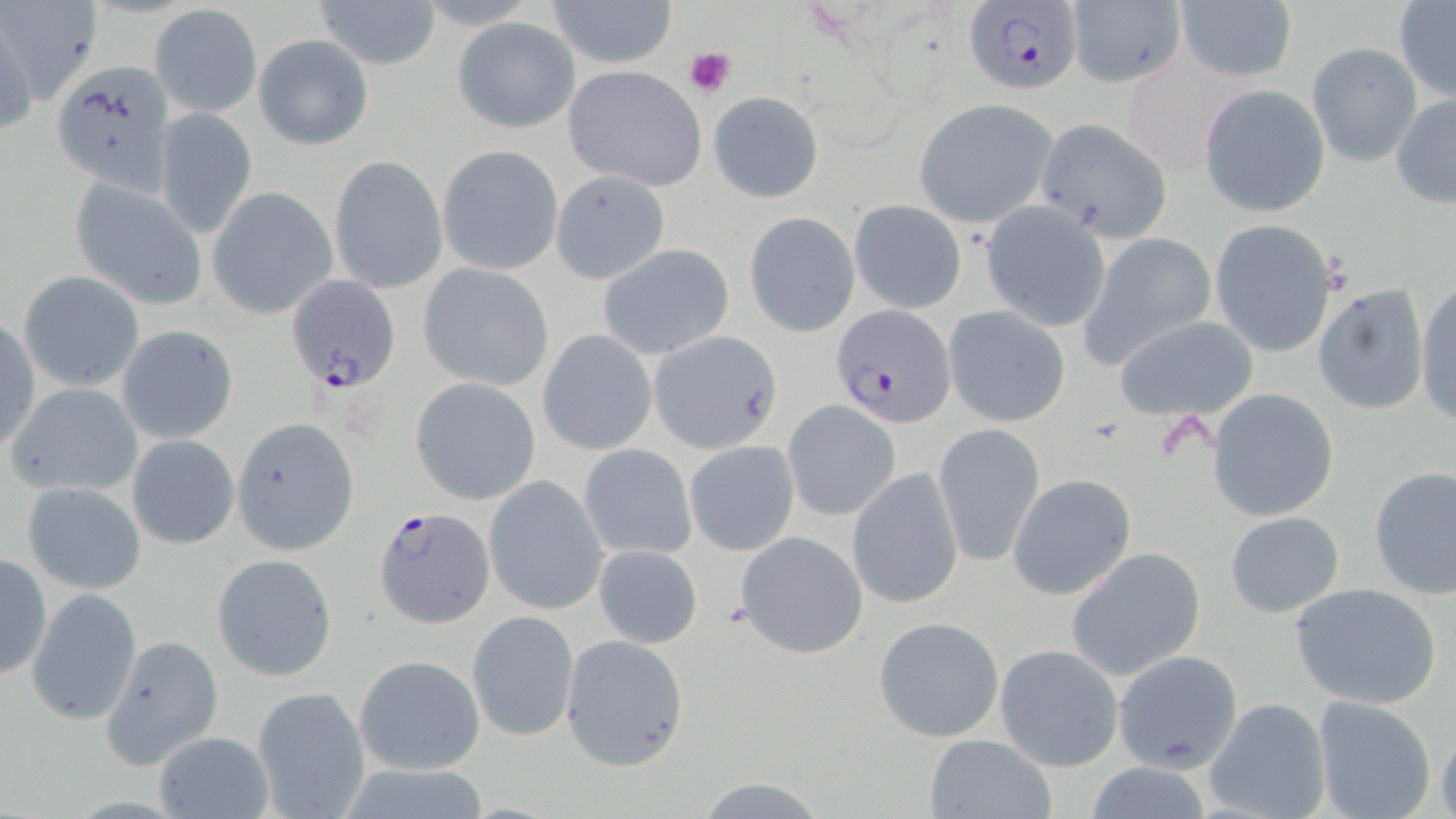 Approximate bounding boxes as (x1, y1, x2, y2) in pixels. Uninfected red blood cell locations: (315, 0, 440, 69), (545, 0, 677, 69), (1065, 0, 1185, 87), (1175, 1, 1297, 83), (1394, 1, 1456, 102), (150, 4, 262, 117), (0, 8, 39, 144), (453, 16, 580, 132), (253, 34, 374, 150), (1307, 42, 1422, 166), (54, 60, 177, 196), (563, 63, 709, 191), (1198, 84, 1330, 218), (708, 90, 824, 203), (1391, 93, 1456, 207), (914, 98, 1058, 229), (156, 108, 259, 237), (1034, 119, 1172, 244), (438, 145, 565, 275), (329, 155, 448, 295), (550, 169, 670, 283), (70, 177, 206, 309), (208, 187, 339, 321), (848, 199, 967, 315), (979, 201, 1111, 333), (743, 212, 860, 337), (1209, 219, 1337, 358), (1080, 234, 1219, 368), (596, 243, 734, 361), (418, 263, 555, 391), (19, 271, 144, 392), (1415, 277, 1456, 428), (1313, 285, 1429, 416), (943, 305, 1070, 427), (1, 313, 38, 453), (1114, 315, 1259, 421), (117, 324, 239, 443), (538, 330, 656, 456), (649, 330, 781, 452), (410, 377, 541, 505), (7, 382, 142, 497), (1206, 388, 1339, 522), (783, 400, 901, 521), (231, 418, 359, 555), (934, 422, 1044, 567), (126, 434, 239, 550), (684, 440, 800, 556), (578, 442, 697, 562), (1369, 466, 1455, 598), (845, 467, 963, 608), (484, 474, 609, 617), (1009, 474, 1136, 600), (22, 481, 147, 595), (1224, 509, 1345, 618), (735, 529, 867, 658), (592, 544, 706, 648), (1066, 546, 1206, 682), (0, 552, 50, 681), (212, 554, 338, 681), (1287, 582, 1443, 709), (27, 589, 140, 724), (467, 610, 578, 741), (874, 616, 1005, 740), (559, 633, 690, 770), (101, 634, 223, 768), (993, 643, 1126, 772), (1112, 648, 1243, 773), (352, 653, 484, 774), (251, 686, 369, 819), (1204, 697, 1331, 819), (1312, 697, 1437, 819), (1436, 726, 1456, 819), (150, 730, 276, 819), (922, 733, 1057, 819), (1082, 759, 1216, 818), (688, 774, 831, 818). Plasmodium falciparum-infected red blood cell locations: (962, 2, 1084, 96), (288, 276, 400, 393), (832, 304, 956, 429), (372, 506, 494, 628). Platelet locations: (684, 46, 737, 97). Slide-level diagnosis: Plasmodium falciparum. May-Grünwald-Giemsa-stained preparation. Image is 1456×819 pixels. One field of a larger specimen. Thin blood smear. Light microscopy. Captured at 1000x magnification.